Assess this cell for malaria.
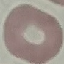
Uninfected.

Thin smear of blood. Giemsa stain. Cell patch, automatically extracted from a larger field of view and resized to 64 × 64 pixels. Photographed with a smartphone camera at the microscope eyepiece.